Assess this cell for malaria.
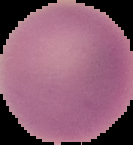
It is uninfected.

image type = cell region segmented out of the field of view; surrounding area masked to black
preparation = thin blood smear
image size = 133×145 pixels